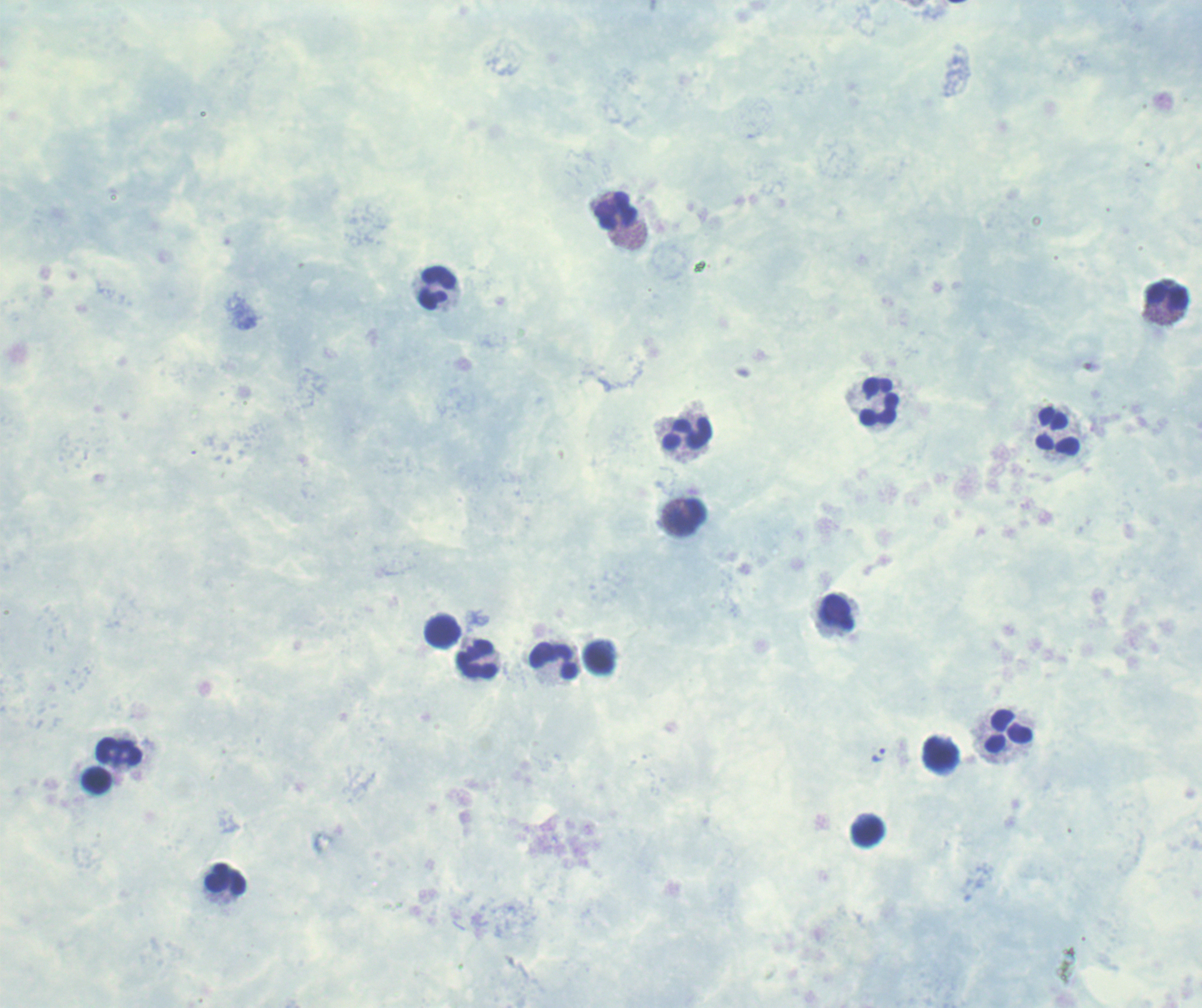

result: positive for Plasmodium parasites
image_size: 1202×1008 pixels
leukocyte_locations: 'approximate centers as [x, y] in pixels: [616, 212], [438, 288], [1168, 297], [880, 402], [1059, 432], [688, 435], [688, 513], [838, 613], [443, 632], [478, 659], [553, 661], [1009, 732], [119, 751], [941, 754], [97, 782], [868, 832], [226, 881]'
magnification: 100x
preparation: thick smear of blood
trophozoite_locations: 'approximate centers as [x, y] in pixels: [879, 756]'
context: previously used in an actual diagnosis
field_of_view: single
background_quality: poor
stain: Romanowsky